Classify this cell by malaria status.
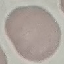

It is uninfected.

Summary:
  - Preparation: thin blood smear
  - Capture: smartphone camera at the microscope eyepiece
  - Stain: Giemsa
  - Image type: cell patch, automatically extracted from a larger field of view and resized to 64 × 64 pixels